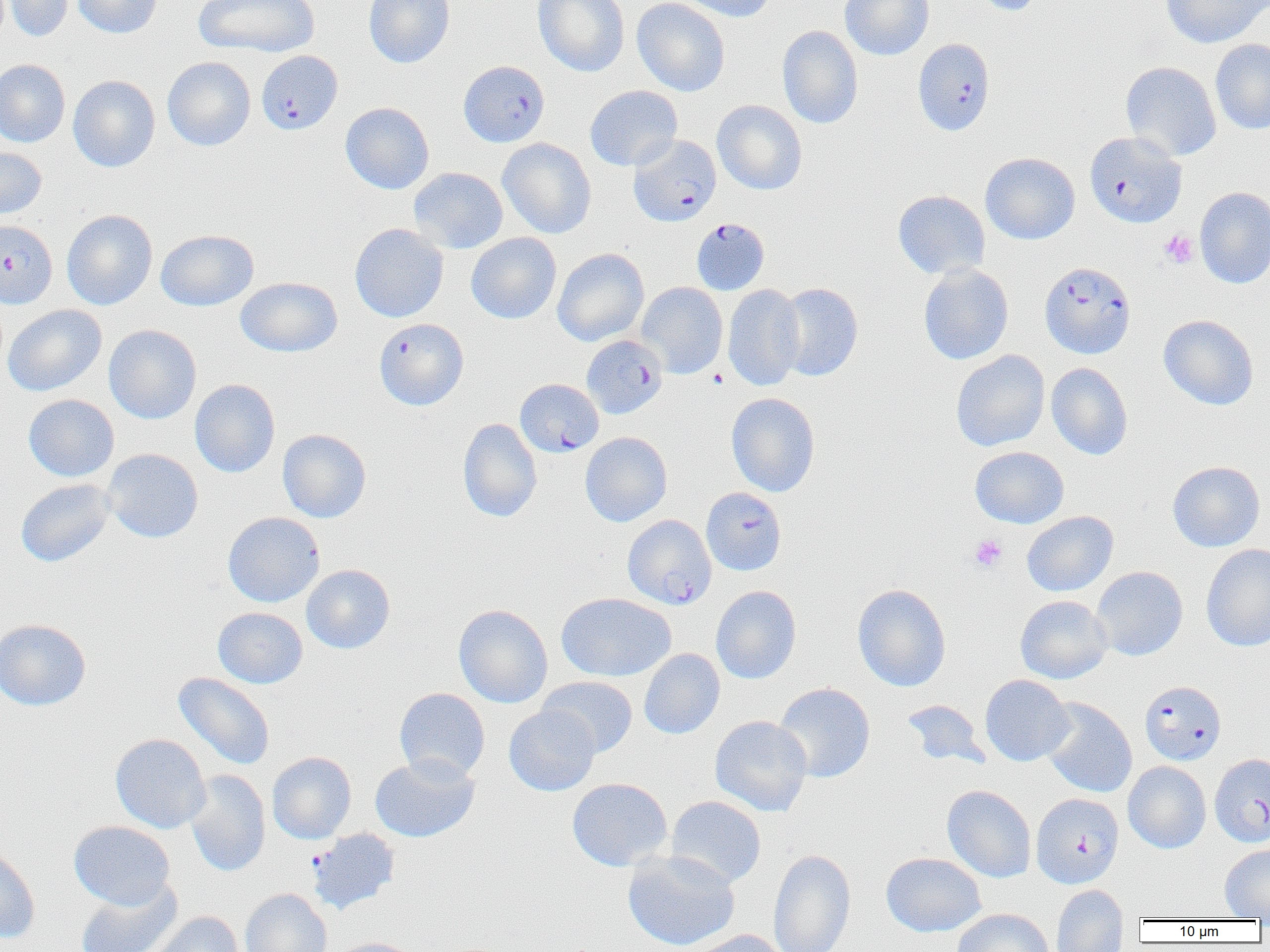
Approximate bounding boxes as named x1/y1/x2/y2 corners in pixels. Platelet locations: (x1=1160, y1=230, x2=1198, y2=269), (x1=969, y1=535, x2=1007, y2=572). Uninfected red blood cell locations (subset): (x1=3, y1=0, x2=74, y2=42), (x1=72, y1=0, x2=162, y2=39), (x1=193, y1=0, x2=320, y2=57), (x1=363, y1=0, x2=455, y2=68), (x1=533, y1=0, x2=630, y2=77), (x1=631, y1=0, x2=730, y2=96), (x1=673, y1=0, x2=775, y2=21), (x1=840, y1=0, x2=934, y2=60), (x1=967, y1=0, x2=1048, y2=16), (x1=1159, y1=0, x2=1269, y2=48), (x1=776, y1=26, x2=864, y2=129), (x1=1210, y1=38, x2=1270, y2=135), (x1=162, y1=57, x2=256, y2=151), (x1=0, y1=59, x2=70, y2=148), (x1=1120, y1=61, x2=1222, y2=161), (x1=68, y1=75, x2=160, y2=172), (x1=585, y1=85, x2=682, y2=171), (x1=712, y1=100, x2=807, y2=194), (x1=340, y1=102, x2=434, y2=194), (x1=497, y1=138, x2=596, y2=238), (x1=0, y1=145, x2=47, y2=219), (x1=980, y1=152, x2=1080, y2=245), (x1=408, y1=167, x2=508, y2=254), (x1=1194, y1=187, x2=1270, y2=288), (x1=893, y1=190, x2=990, y2=279), (x1=61, y1=209, x2=158, y2=310), (x1=349, y1=223, x2=449, y2=322), (x1=156, y1=229, x2=258, y2=311), (x1=466, y1=232, x2=561, y2=324), (x1=552, y1=247, x2=649, y2=346), (x1=918, y1=265, x2=1014, y2=365), (x1=236, y1=276, x2=342, y2=357), (x1=636, y1=282, x2=728, y2=378), (x1=775, y1=283, x2=863, y2=381), (x1=722, y1=284, x2=805, y2=391), (x1=3, y1=304, x2=106, y2=396), (x1=1158, y1=314, x2=1258, y2=410), (x1=104, y1=325, x2=201, y2=424), (x1=951, y1=350, x2=1050, y2=452), (x1=1046, y1=363, x2=1132, y2=460), (x1=190, y1=379, x2=280, y2=477), (x1=726, y1=392, x2=820, y2=497), (x1=23, y1=394, x2=119, y2=481), (x1=458, y1=418, x2=542, y2=522), (x1=277, y1=429, x2=371, y2=523), (x1=580, y1=431, x2=672, y2=526), (x1=969, y1=446, x2=1069, y2=528), (x1=102, y1=448, x2=203, y2=543), (x1=1167, y1=461, x2=1265, y2=552), (x1=15, y1=479, x2=116, y2=567), (x1=223, y1=511, x2=324, y2=607), (x1=1022, y1=511, x2=1118, y2=597), (x1=1201, y1=544, x2=1270, y2=652), (x1=301, y1=564, x2=395, y2=654), (x1=1091, y1=566, x2=1188, y2=661), (x1=852, y1=583, x2=951, y2=692), (x1=711, y1=585, x2=802, y2=684), (x1=556, y1=592, x2=676, y2=682), (x1=1015, y1=595, x2=1112, y2=684), (x1=453, y1=603, x2=553, y2=708), (x1=212, y1=607, x2=308, y2=688), (x1=0, y1=618, x2=91, y2=710), (x1=639, y1=649, x2=725, y2=739), (x1=173, y1=672, x2=275, y2=770), (x1=980, y1=674, x2=1074, y2=766), (x1=538, y1=676, x2=638, y2=758), (x1=774, y1=682, x2=876, y2=783), (x1=394, y1=688, x2=490, y2=782), (x1=1040, y1=698, x2=1137, y2=797), (x1=900, y1=699, x2=990, y2=769), (x1=504, y1=705, x2=599, y2=795), (x1=710, y1=715, x2=812, y2=816), (x1=110, y1=733, x2=211, y2=833), (x1=267, y1=751, x2=357, y2=844), (x1=370, y1=754, x2=480, y2=843), (x1=1123, y1=761, x2=1211, y2=853), (x1=184, y1=769, x2=270, y2=876), (x1=567, y1=777, x2=672, y2=872), (x1=942, y1=785, x2=1036, y2=883), (x1=665, y1=796, x2=766, y2=888), (x1=69, y1=821, x2=175, y2=910), (x1=0, y1=843, x2=40, y2=944), (x1=1220, y1=844, x2=1270, y2=919), (x1=768, y1=848, x2=856, y2=952), (x1=622, y1=849, x2=741, y2=951), (x1=881, y1=852, x2=986, y2=936), (x1=75, y1=878, x2=183, y2=952), (x1=1051, y1=884, x2=1128, y2=952), (x1=240, y1=889, x2=332, y2=952), (x1=952, y1=908, x2=1054, y2=952), (x1=144, y1=911, x2=244, y2=952), (x1=685, y1=929, x2=790, y2=952), (x1=328, y1=937, x2=424, y2=952). Plasmodium falciparum-infected red blood cell locations (subset): (x1=913, y1=40, x2=995, y2=137), (x1=257, y1=50, x2=343, y2=134), (x1=459, y1=60, x2=549, y2=147), (x1=1085, y1=131, x2=1187, y2=227), (x1=628, y1=135, x2=721, y2=226), (x1=692, y1=218, x2=770, y2=295), (x1=2, y1=222, x2=59, y2=312), (x1=1040, y1=261, x2=1135, y2=359), (x1=374, y1=318, x2=469, y2=410), (x1=583, y1=333, x2=669, y2=417), (x1=515, y1=379, x2=604, y2=457), (x1=701, y1=487, x2=786, y2=576), (x1=1140, y1=681, x2=1226, y2=765), (x1=1211, y1=752, x2=1270, y2=846), (x1=1032, y1=793, x2=1124, y2=888), (x1=307, y1=829, x2=400, y2=915). Slide-level diagnosis: Plasmodium falciparum. Image is 1270×952 pixels. Single field of view. 1000x magnification. Light microscopy. Thin blood smear.